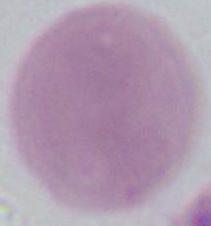

{
  "modality": "photomicrograph",
  "identification": "red blood cell",
  "magnification": "1000x"
}